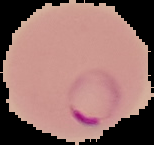
malaria status = parasitized
image size = 154×145 pixels
preparation = thin blood film
image type = segmented cell region on a black background